Classify this cell by malaria status.
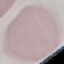

It is uninfected.

preparation: thin smear
image_type: automatically extracted cell patch, resized to 64 × 64 pixels
stain: Giemsa
capture: smartphone camera at the microscope eyepiece